Assess this cell for malaria.
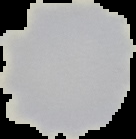

It is uninfected.

preparation = thin blood film
image type = segmented cell region on a black background
image size = 136×139 pixels